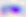
Summary:
  - Magnification: 400x
  - Modality: micrograph
  - Identification: Toxoplasma gondii